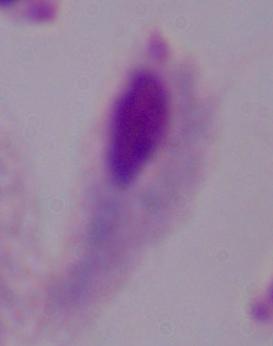

Photomicrograph. Captured at 1000x magnification. A trichomonad is seen.